Point out malaria parasites and leukocytes.
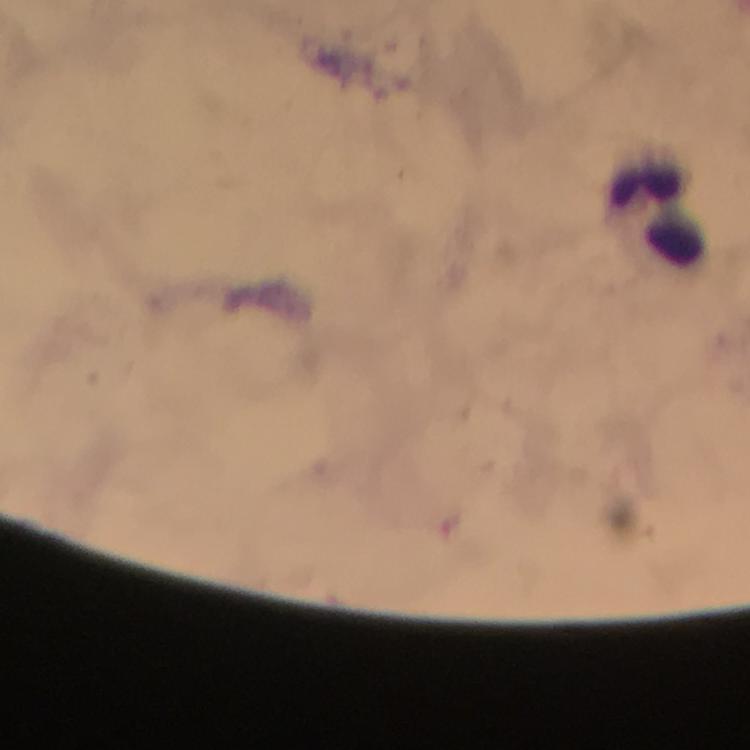

No malaria parasites detected.
Approximate centers as {x, y} in pixels.
Leukocytes: {658, 207}.

Summary:
  - Stain: Giemsa
  - Immersion oil: applied
  - Context: from a diagnostic examination for malaria
  - Capture: smartphone mounted on the microscope
  - Image size: 750×750 pixels
  - Cropped from: a single field of view
  - Preparation: thick blood film
  - Magnification: 100x